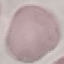
Summary:
  - Result: negative for malaria parasites
  - Stain: Giemsa
  - Capture: smartphone camera at the microscope eyepiece
  - Preparation: thin blood smear
  - Image type: cell patch, automatically extracted from a larger field of view and resized to 64 × 64 pixels